Classify this cell by malaria status.
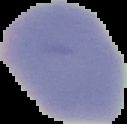

It is uninfected.

Summary:
  - Image size: 127×124 pixels
  - Image type: segmented cell region with the area outside set to black
  - Preparation: thin blood film